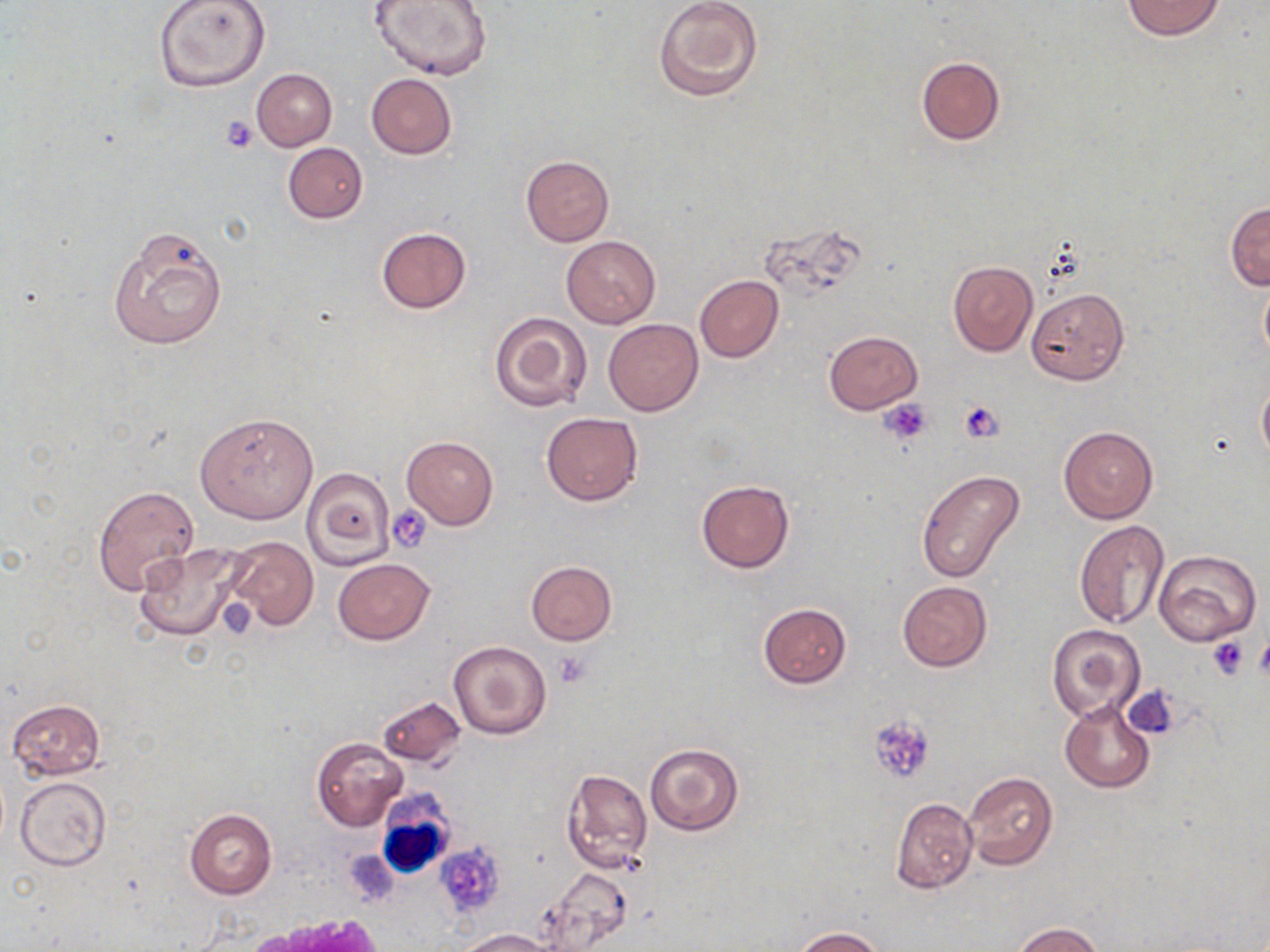
Summary:
  - Coordinate format: approximate bounding boxes as [x1, y1, x2, y2] in pixels
  - Platelet locations: [221, 116, 259, 153], [878, 397, 934, 446], [959, 400, 1005, 444], [388, 506, 435, 554], [1255, 636, 1270, 684], [1209, 638, 1250, 681], [555, 651, 591, 686], [1123, 686, 1181, 741], [869, 716, 934, 785]
  - Uninfected red blood cell locations: [152, 0, 272, 92], [371, 0, 494, 80], [653, 0, 764, 103], [1122, 1, 1225, 40], [915, 55, 1005, 146], [251, 68, 336, 151], [366, 74, 456, 159], [282, 142, 367, 223], [520, 155, 614, 247], [1225, 201, 1270, 290], [763, 221, 868, 304], [107, 226, 228, 348], [376, 227, 472, 313], [561, 236, 661, 328], [947, 260, 1038, 356], [694, 275, 783, 362], [1258, 275, 1270, 363], [1027, 288, 1128, 386], [488, 310, 593, 412], [604, 318, 703, 416], [823, 331, 924, 415], [1257, 383, 1270, 467], [195, 410, 320, 525], [541, 412, 642, 505], [1058, 426, 1158, 523], [402, 434, 498, 530], [301, 468, 395, 572], [915, 469, 1024, 581], [695, 480, 794, 573], [92, 485, 200, 595], [1073, 521, 1170, 630], [226, 536, 318, 631], [133, 541, 251, 643], [1154, 549, 1261, 645], [333, 558, 434, 645], [525, 561, 618, 644], [897, 580, 993, 672], [757, 602, 851, 689], [1047, 623, 1146, 724], [447, 641, 550, 739], [377, 695, 467, 768], [7, 698, 106, 779], [1059, 700, 1156, 793], [312, 736, 408, 830], [644, 743, 744, 835], [563, 768, 652, 872], [963, 772, 1058, 872], [16, 777, 110, 869], [889, 798, 978, 894], [184, 809, 277, 899], [435, 841, 504, 918], [542, 869, 632, 946], [1011, 923, 1106, 952], [791, 927, 884, 951], [459, 929, 555, 952]
  - White blood cell locations: [375, 784, 454, 879]
  - Slide-level diagnosis: no evidence of blood parasites
  - Modality: optical microscopy
  - Preparation: thin blood smear
  - Field of view: one of a larger specimen
  - Stain: May-Grünwald-Giemsa
  - Image size: 1270×952 pixels
  - Magnification: 1000x